Report the malaria status of this cell.
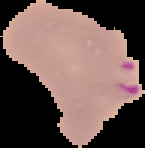

Parasitized.

Segmented cell region on a black background. Image is 145×148 pixels. From a thin blood film.